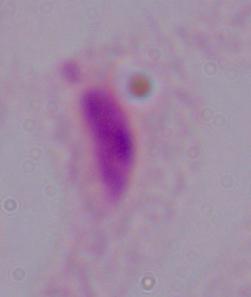
A trichomonad is seen. Micrograph. 1000x magnification.